Mark where platelets are.
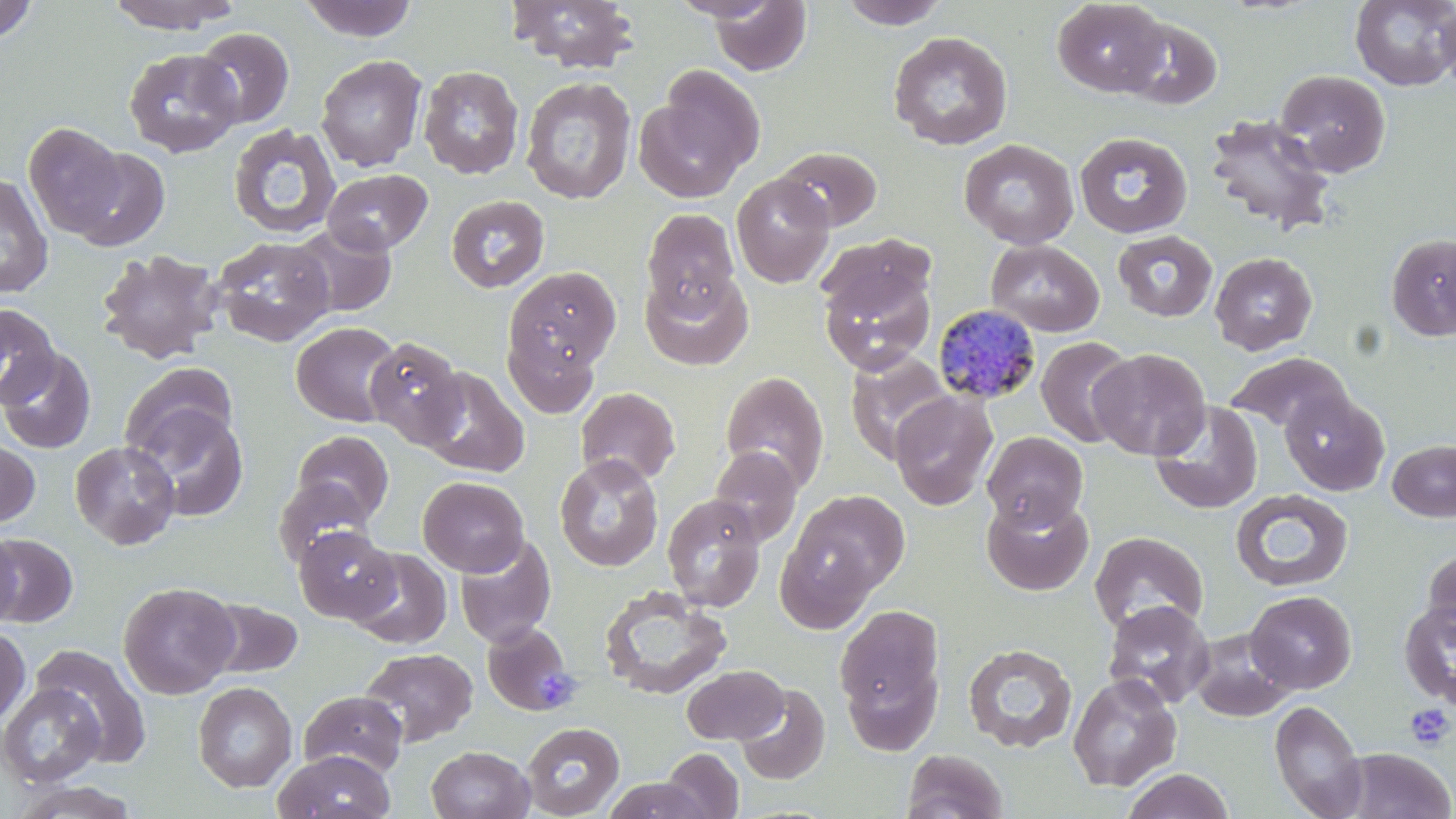

Approximate bounding boxes as (x1,y1)-(x2,y2) corner pairs in pixels.
Platelets: (535,666)-(576,713), (1405,704)-(1454,751).

slide-level diagnosis = Plasmodium malariae
image size = 1456×819 pixels
field of view = single
preparation = thin blood film
stain = May-Grünwald-Giemsa
Plasmodium malariae-infected red blood cell locations = approximate bounding boxes as (x1,y1)-(x2,y2) corner pairs in pixels: (932,303)-(1044,405)
magnification = 1000x
modality = optical microscopy
uninfected red blood cell locations = approximate bounding boxes as (x1,y1)-(x2,y2) corner pairs in pixels: (0,0)-(38,43), (106,0)-(241,33), (299,0)-(419,42), (506,0)-(641,74), (836,0)-(951,29), (1052,0)-(1170,97), (1350,0)-(1456,91), (707,1)-(812,76), (1435,3)-(1456,91), (1117,15)-(1223,111), (192,27)-(294,128), (888,31)-(1013,151), (124,48)-(242,157), (315,54)-(427,171), (418,65)-(524,179), (1275,69)-(1391,177), (521,76)-(637,204), (634,78)-(761,204), (1204,113)-(1337,235), (23,122)-(126,238), (228,124)-(340,240), (1074,131)-(1193,239), (959,138)-(1079,249), (776,146)-(882,232), (66,147)-(170,252), (323,169)-(432,255), (0,173)-(53,298), (731,173)-(835,288), (446,195)-(550,293), (642,208)-(739,313), (289,222)-(398,318), (1112,230)-(1218,321), (815,232)-(935,318), (1386,233)-(1456,341), (212,236)-(335,347), (986,239)-(1104,337), (96,249)-(225,365), (1209,252)-(1317,355), (819,263)-(937,374), (503,266)-(621,383), (640,269)-(754,370), (0,304)-(60,407), (291,321)-(403,427), (503,327)-(602,418), (365,336)-(468,449), (1036,336)-(1136,448), (0,347)-(96,453), (1088,348)-(1210,460), (846,350)-(952,463), (1225,352)-(1353,435), (118,362)-(239,462), (419,367)-(530,478), (720,371)-(829,492), (575,387)-(681,486), (1281,390)-(1389,496), (889,391)-(997,510), (126,399)-(251,523), (1150,401)-(1263,514), (293,430)-(393,524), (982,431)-(1088,529), (0,438)-(40,528), (1388,439)-(1456,522), (69,441)-(180,549), (708,446)-(802,547), (555,454)-(664,572), (418,476)-(529,576), (273,477)-(373,569), (1231,488)-(1353,592), (784,489)-(910,605), (662,494)-(766,612), (981,494)-(1094,596), (294,525)-(398,624), (0,531)-(23,629), (1089,531)-(1209,636), (2,532)-(78,627), (454,534)-(556,647), (1422,546)-(1456,648), (347,547)-(452,649), (118,581)-(240,699), (599,585)-(732,700), (1245,590)-(1357,694), (202,597)-(304,679), (1103,601)-(1215,708), (1398,601)-(1456,708), (834,603)-(945,730), (481,621)-(576,716), (0,625)-(31,729), (1190,628)-(1297,721), (963,644)-(1078,752), (33,645)-(152,764), (360,647)-(478,747), (842,659)-(942,757), (682,664)-(788,744), (1067,673)-(1182,792), (193,681)-(297,793), (0,683)-(104,788), (735,683)-(830,785), (299,691)-(407,776), (1270,699)-(1367,818), (522,721)-(625,818), (427,745)-(534,819), (660,747)-(744,818), (1334,747)-(1456,819), (902,749)-(1008,819), (273,750)-(396,819), (1121,768)-(1236,819), (603,777)-(712,819), (10,780)-(141,818)